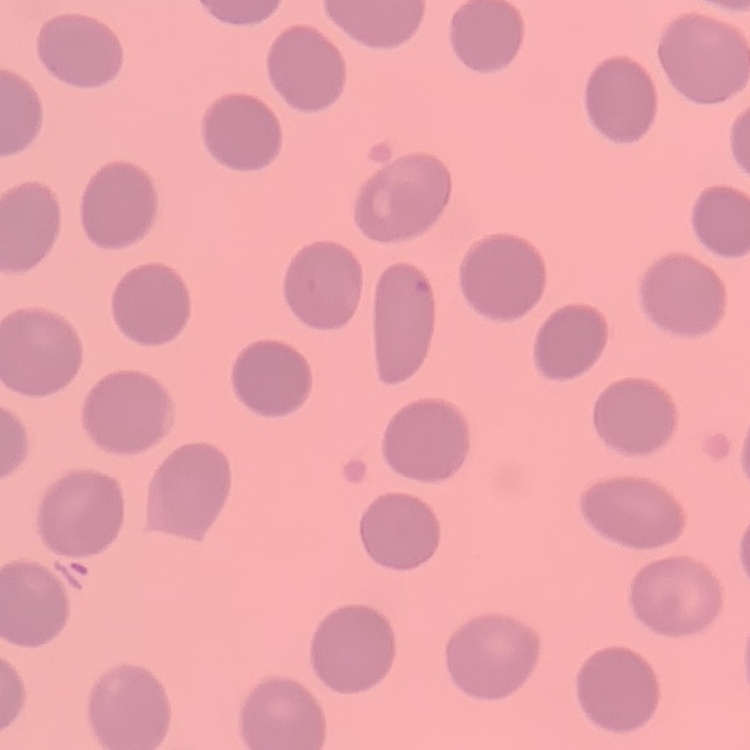
The erythrocytes exhibit no rouleaux formation. One tile cut from a larger photomicrograph. Thin peripheral smear. Stained with either Field's or Giemsa.